Locate every Plasmodium parasite by life-cycle stage, and every leukocyte.
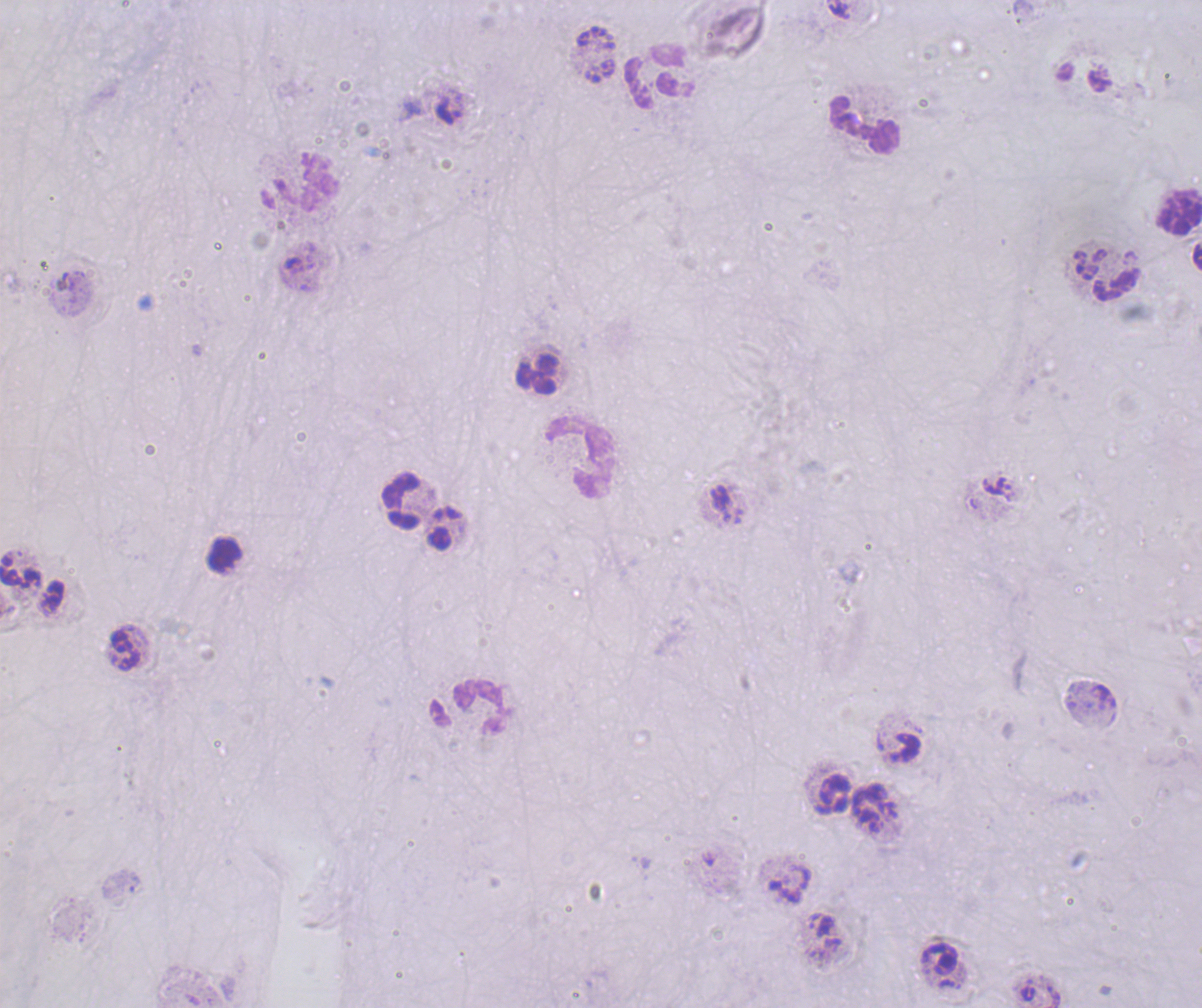

No Plasmodium parasites seen.
Approximate centers as {x, y} in pixels.
Leukocytes: {660, 76}, {863, 125}, {298, 182}, {1177, 213}, {538, 374}, {581, 457}, {402, 502}, {224, 555}, {123, 652}, {466, 708}.

background quality = poor
context = previously used in a real diagnosis
field of view = single
image size = 1202×1008 pixels
coloration quality = bad
magnification = 100x
preparation = thick blood film
stain = Romanowsky